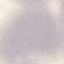

Summary:
  - Malaria status: uninfected
  - Preparation: thin smear
  - Stain: Giemsa
  - Image type: automatically extracted cell patch, resized to 64 × 64 pixels
  - Capture: smartphone through the microscope eyepiece